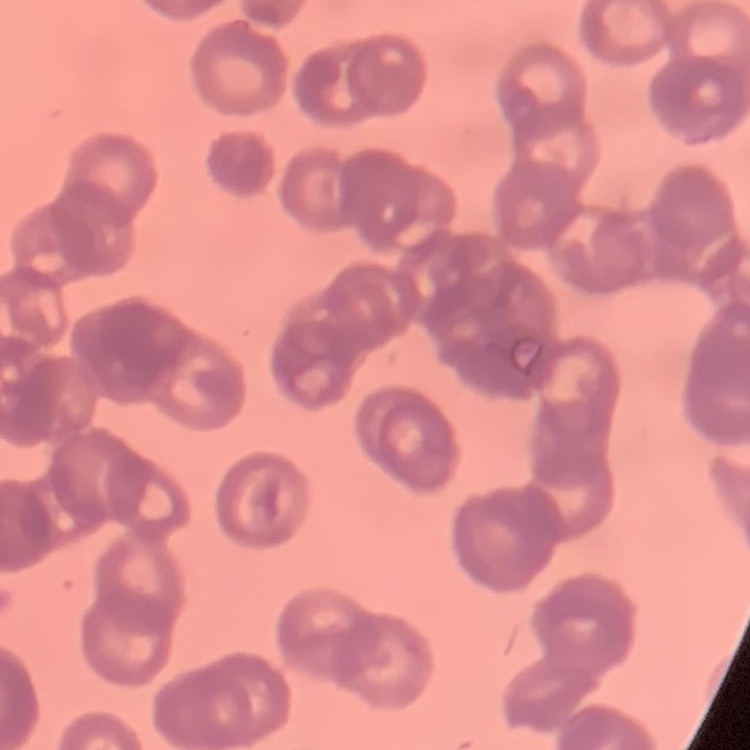

The red blood cells exhibit rouleaux formation. Stained with either Field's or Giemsa. One tile cut from a larger photomicrograph. Thin blood smear.